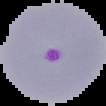 Image is 106×106 pixels. Segmented cell region on a black background. Result: malaria parasites detected. From a thin blood smear.